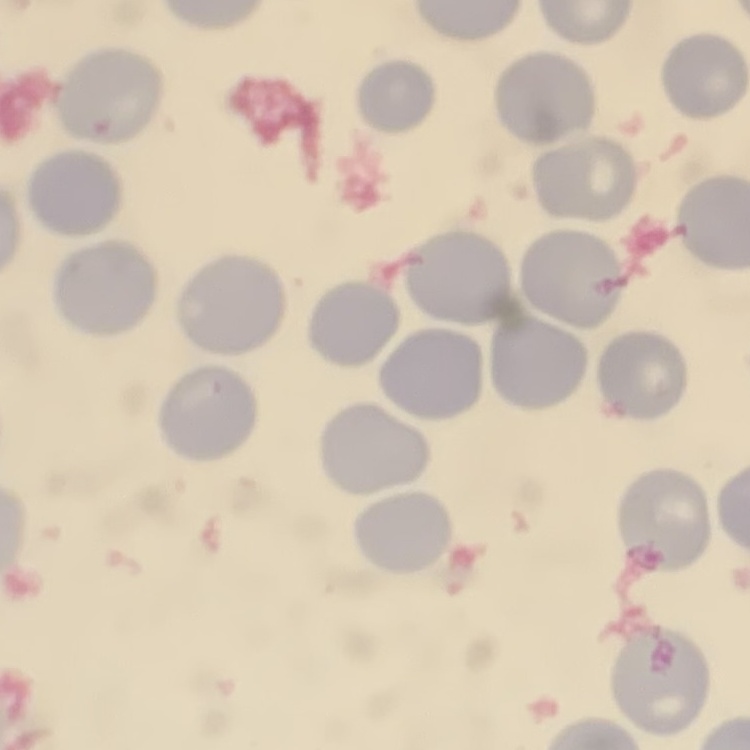 The red blood cells exhibit no rouleaux formation. Thin peripheral smear. Field's or Giemsa stain. One tile cut from a larger photomicrograph.